Assess this cell for malaria.
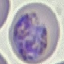
It is parasitized.

Photographed with a smartphone camera at the microscope eyepiece. Giemsa-stained preparation. Cell patch, automatically extracted from a larger field of view and resized to 64 × 64 pixels. Thin smear of blood.